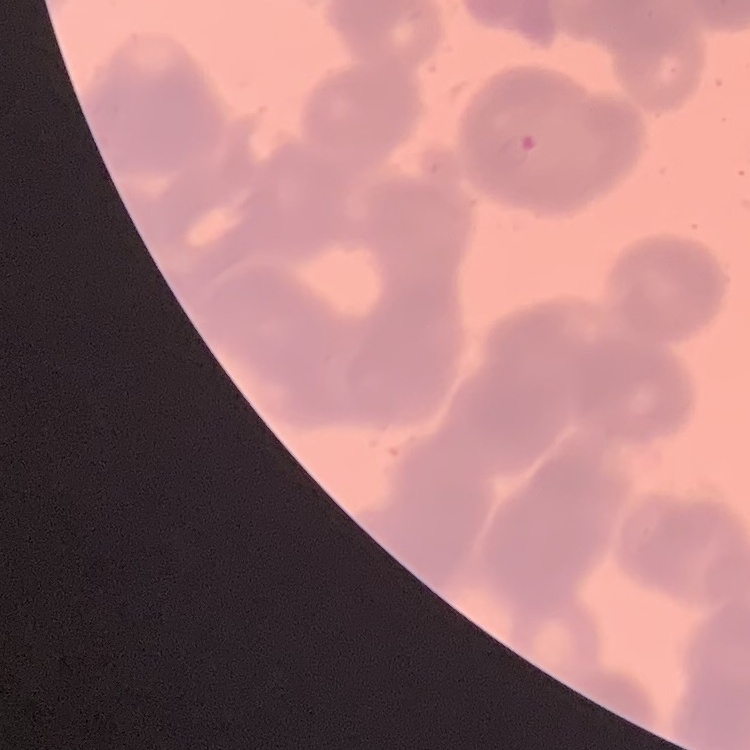
Summary:
  - Erythrocyte morphology: rouleaux formation
  - Stain: Field's or Giemsa
  - Preparation: thin blood smear
  - Image type: one tile cut from a larger photomicrograph